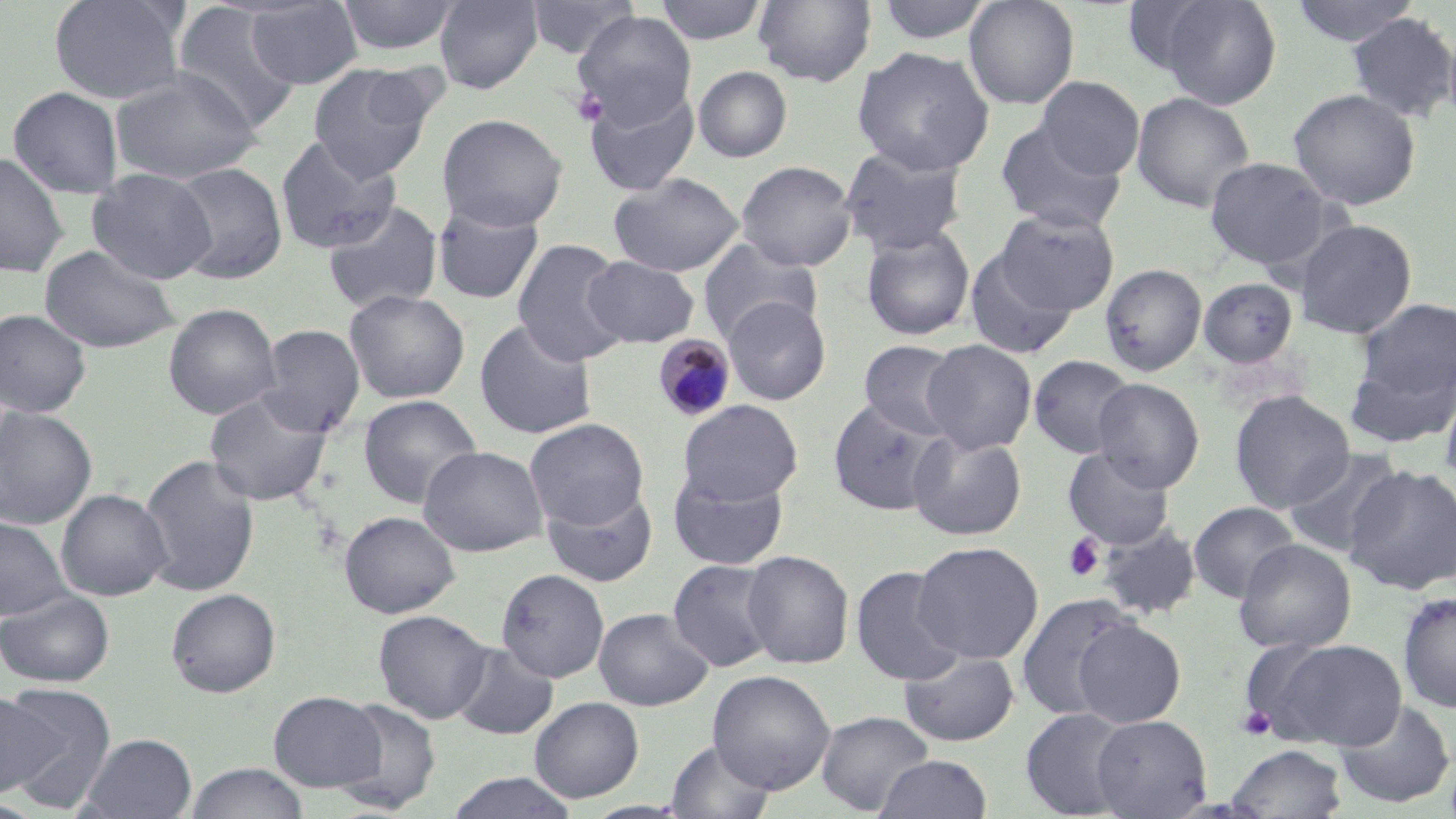
slide-level diagnosis = Plasmodium malariae
stain = May-Grünwald-Giemsa
image size = 1456×819 pixels
field of view = single
platelet locations = approximate bounding boxes as [x1, y1, x2, y2] in pixels: [570, 87, 609, 128], [1063, 533, 1105, 582], [1237, 705, 1277, 741]
magnification = 1000x
modality = light microscopy
uninfected red blood cell locations = approximate bounding boxes as [x1, y1, x2, y2] in pixels: [48, 0, 189, 105], [245, 0, 362, 89], [337, 0, 459, 55], [434, 0, 544, 94], [526, 0, 638, 60], [655, 0, 767, 45], [753, 0, 876, 87], [874, 0, 994, 45], [964, 0, 1079, 110], [1120, 0, 1223, 78], [1156, 0, 1282, 109], [1289, 0, 1422, 48], [172, 3, 302, 134], [572, 10, 697, 128], [1346, 12, 1456, 123], [852, 46, 994, 176], [308, 65, 437, 183], [693, 66, 792, 163], [110, 68, 262, 184], [1036, 76, 1144, 180], [8, 86, 123, 199], [584, 86, 700, 196], [1289, 88, 1420, 211], [1131, 91, 1256, 213], [437, 113, 567, 231], [995, 119, 1128, 235], [275, 135, 401, 255], [839, 146, 968, 257], [0, 151, 69, 277], [1204, 157, 1331, 270], [737, 160, 857, 271], [167, 162, 287, 285], [88, 169, 216, 285], [608, 172, 744, 277], [322, 199, 443, 315], [432, 204, 545, 305], [996, 208, 1119, 315], [1294, 218, 1418, 338], [860, 226, 976, 342], [697, 238, 822, 345], [513, 239, 629, 367], [39, 244, 180, 354], [965, 251, 1078, 360], [583, 256, 700, 347], [1100, 263, 1207, 377], [1199, 279, 1298, 368], [344, 289, 470, 404], [723, 296, 831, 405], [1354, 297, 1456, 401], [163, 303, 281, 420], [0, 308, 91, 417], [474, 318, 598, 440], [258, 324, 364, 437], [922, 339, 1036, 455], [859, 340, 967, 441], [1345, 353, 1456, 450], [1029, 355, 1137, 458], [1093, 378, 1205, 493], [1439, 381, 1456, 492], [204, 388, 333, 506], [1230, 389, 1354, 513], [358, 395, 482, 510], [828, 398, 947, 516], [678, 399, 803, 505], [0, 406, 98, 529], [525, 418, 649, 532], [908, 430, 1027, 541], [418, 445, 547, 557], [1063, 445, 1175, 550], [1282, 446, 1406, 561], [139, 454, 260, 597], [1345, 464, 1456, 595], [669, 469, 789, 570], [542, 486, 658, 587], [56, 489, 173, 601], [1188, 501, 1300, 602], [339, 511, 460, 618], [0, 517, 71, 621], [1096, 521, 1202, 621], [1233, 539, 1356, 654], [912, 541, 1043, 665], [742, 550, 854, 669], [668, 559, 779, 672], [851, 565, 965, 686], [496, 568, 609, 683], [166, 588, 281, 697], [0, 589, 115, 688], [1397, 591, 1456, 713], [1016, 593, 1141, 721], [593, 607, 713, 711], [373, 609, 493, 724], [1071, 618, 1186, 727], [1262, 637, 1407, 751], [451, 642, 557, 739], [899, 649, 1019, 747], [708, 669, 835, 795], [1, 684, 116, 813], [268, 691, 385, 793], [530, 696, 644, 802], [331, 699, 442, 814], [1334, 699, 1455, 809], [1020, 707, 1136, 819], [815, 710, 934, 816], [1091, 714, 1212, 818], [79, 733, 197, 818], [666, 739, 775, 818], [1227, 743, 1347, 818], [874, 754, 993, 818], [184, 761, 309, 819], [445, 771, 579, 819], [0, 796, 47, 818]
preparation = thin blood film
Plasmodium malariae-infected red blood cell locations = approximate bounding boxes as [x1, y1, x2, y2] in pixels: [653, 334, 736, 421]